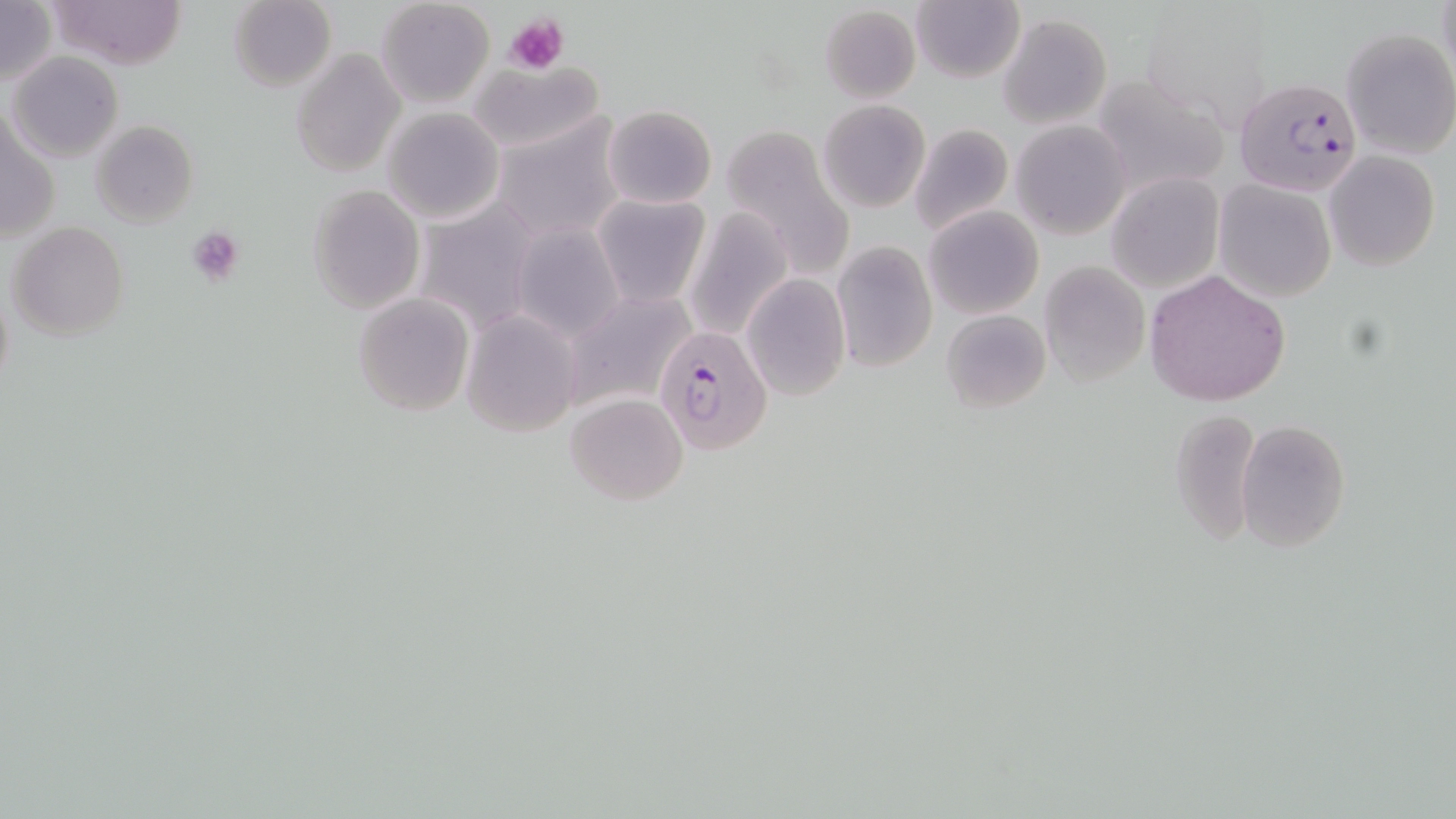

slide_level_diagnosis: Plasmodium falciparum
field_of_view: one of a larger specimen
plasmodium_falciparum_infected_red_blood_cell_locations: 'approximate bounding boxes as (x1, y1, x2, y2) in pixels: (1234, 76, 1364, 200), (656, 325, 772, 455)'
platelet_locations: 'approximate bounding boxes as (x1, y1, x2, y2) in pixels: (505, 13, 566, 75), (187, 225, 245, 288)'
image_size: 1456×819 pixels
modality: light microscopy
magnification: 1000x
preparation: thin blood smear
stain: May-Grünwald-Giemsa
uninfected_red_blood_cell_locations: 'approximate bounding boxes as (x1, y1, x2, y2) in pixels: (0, 0, 56, 89), (50, 0, 187, 70), (229, 0, 337, 90), (375, 0, 496, 110), (910, 2, 1024, 83), (818, 4, 923, 103), (1140, 7, 1275, 129), (998, 14, 1111, 128), (1340, 28, 1456, 160), (292, 46, 405, 178), (6, 52, 124, 162), (468, 60, 602, 154), (1088, 74, 1228, 196), (817, 100, 930, 214), (603, 105, 717, 209), (381, 107, 505, 225), (491, 114, 628, 243), (2, 115, 57, 247), (89, 120, 198, 228), (909, 120, 1016, 237), (1011, 120, 1131, 238), (724, 129, 855, 282), (1323, 151, 1441, 272), (1106, 173, 1223, 292), (1214, 180, 1337, 301), (308, 184, 427, 314), (591, 193, 710, 310), (325, 197, 451, 394), (415, 201, 544, 332), (924, 205, 1044, 319), (682, 208, 794, 342), (7, 221, 128, 339), (510, 221, 626, 342), (831, 242, 936, 373), (1039, 260, 1151, 387), (1144, 269, 1290, 406), (740, 273, 850, 401), (558, 288, 698, 413), (352, 293, 474, 416), (941, 308, 1051, 412), (461, 310, 582, 437), (564, 392, 689, 505), (1168, 407, 1261, 547), (1236, 419, 1351, 552)'